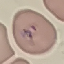

Summary:
  - Result: malaria parasites detected
  - Capture: smartphone through the microscope eyepiece
  - Image type: cell patch, automatically extracted from a larger field of view and resized to 64 × 64 pixels
  - Preparation: thin blood film
  - Stain: Giemsa